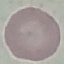

Result: no malaria parasites detected. Thin blood smear. Acquired by smartphone through the microscope eyepiece. Cell patch, automatically extracted from a larger field of view and resized to 64 × 64 pixels. Giemsa-stained preparation.